Locate every Plasmodium falciparum-infected red blood cell.
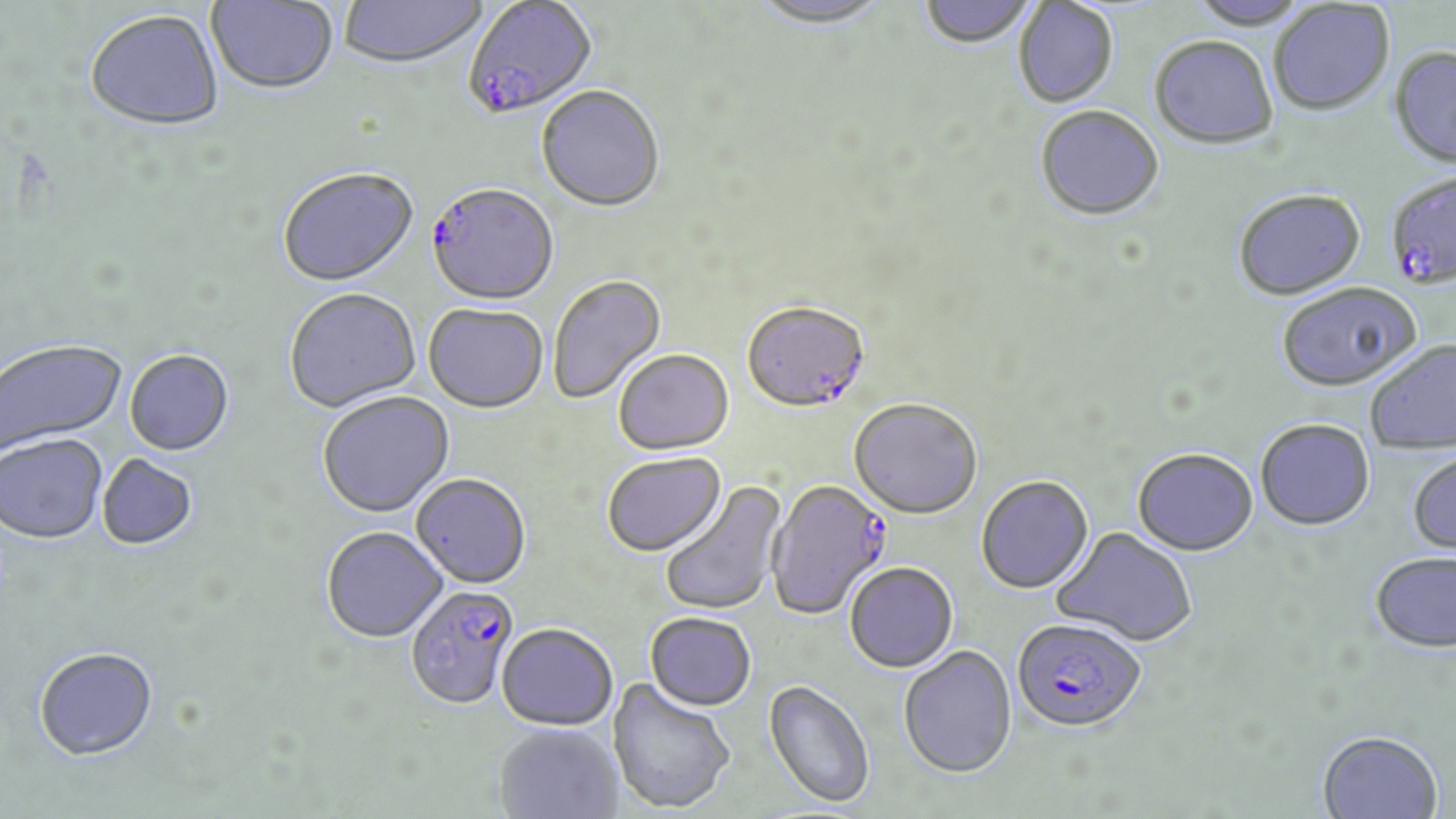

Approximate bounding boxes as (x1,y1)-(x2,y2) corner pairs in pixels.
Plasmodium falciparum-infected red blood cells: (462,2)-(598,122), (1390,171)-(1456,290), (427,186)-(559,308), (742,304)-(871,416), (766,481)-(892,622), (405,586)-(519,712), (1012,619)-(1146,735).

Uninfected red blood cell locations: (206,0)-(338,97), (919,0)-(1038,51), (339,1)-(487,71), (746,1)-(894,32), (1186,1)-(1310,31), (1013,2)-(1119,109), (1269,2)-(1395,118), (85,12)-(224,134), (1149,38)-(1278,151), (1388,49)-(1456,171), (536,87)-(665,214), (1035,108)-(1165,223), (278,169)-(420,290), (1233,191)-(1367,302), (548,275)-(667,405), (1276,285)-(1422,395), (284,290)-(422,415), (423,305)-(548,415), (1,341)-(127,457), (1366,341)-(1456,454), (125,351)-(235,457), (614,351)-(734,457), (318,393)-(457,520), (848,401)-(982,522), (1255,421)-(1375,533), (0,435)-(108,547), (1132,451)-(1258,559), (602,454)-(727,558), (1407,454)-(1456,558), (97,455)-(198,552), (410,476)-(531,590), (976,477)-(1094,596), (659,481)-(787,617), (1049,527)-(1198,648), (321,528)-(448,645), (1370,554)-(1456,656), (845,564)-(959,674), (644,614)-(756,713), (496,625)-(618,731), (898,646)-(1018,781), (34,649)-(159,765), (606,677)-(736,815), (763,680)-(875,810), (493,724)-(624,818), (1316,731)-(1443,819). Slide-level diagnosis: Plasmodium falciparum. Thin blood film. Image is 1456×819 pixels. Optical microscopy. 1000x magnification. May-Grünwald-Giemsa-stained preparation. Single field of view.